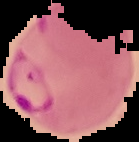

Summary:
  - Preparation: thin blood smear
  - Malaria status: parasitized
  - Image size: 139×142 pixels
  - Image type: cell region segmented out of the field of view; surrounding area masked to black